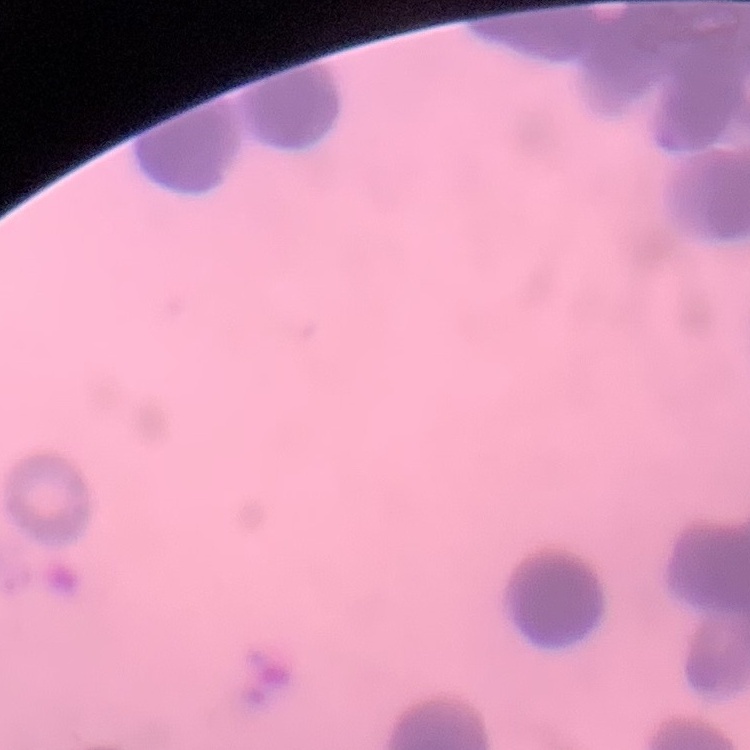

Summary:
  - Red blood cell morphology: rouleaux formation
  - Stain: Field's or Giemsa
  - Image type: one tile cut from a larger photomicrograph
  - Preparation: thin blood film